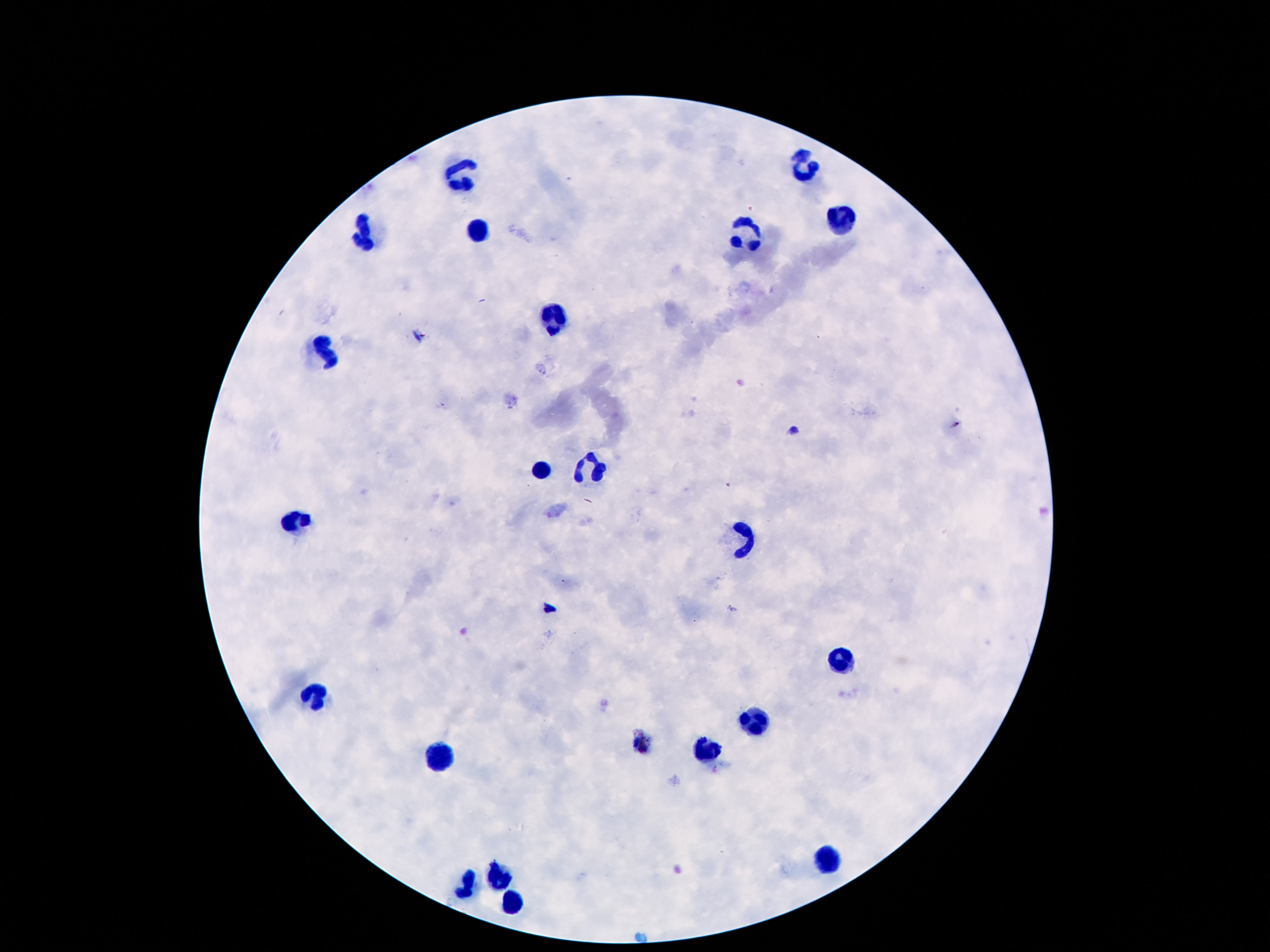
Approximate centers as [x, y] in pixels.
Summary:
  - Leukocyte locations: [804, 166], [463, 172], [836, 222], [478, 226], [746, 232], [364, 234], [552, 322], [325, 358], [595, 467], [543, 470], [291, 523], [744, 540], [841, 655], [317, 697], [754, 721], [707, 751], [440, 757], [828, 860], [500, 872], [468, 889], [513, 900]
  - Stain: Giemsa
  - Capture: smartphone camera through the microscope eyepiece
  - Field of view: single
  - Image size: 1270×952 pixels
  - Patient malaria status: uninfected
  - Magnification: 100x
  - Preparation: thick peripheral-blood smear